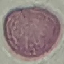

Result: no malaria parasites detected. Thin blood film. Photographed with a smartphone camera at the microscope eyepiece. Giemsa stain. Automatically extracted cell patch, resized to 64 × 64 pixels.